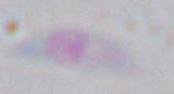

Summary:
  - Modality: photomicrograph
  - Magnification: 1000x
  - Identification: Toxoplasma gondii